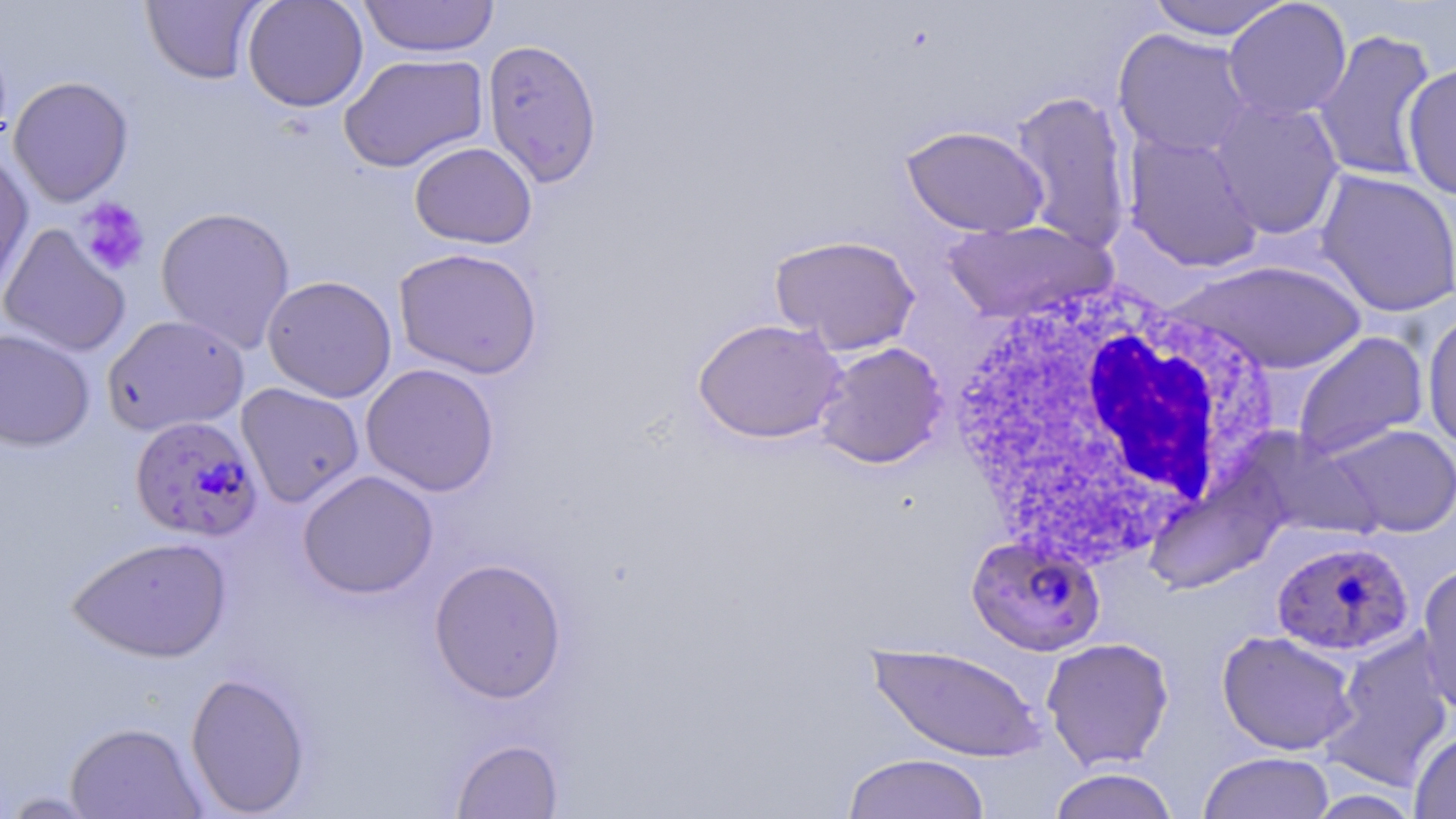 Approximate bounding boxes as (x1, y1, x2, y2) in pixels. White blood cell locations: (941, 271, 1284, 572). Plasmodium falciparum-infected red blood cell locations: (124, 415, 258, 542), (966, 533, 1106, 656), (1271, 539, 1414, 657). Uninfected red blood cell locations: (140, 0, 267, 85), (242, 0, 368, 112), (358, 0, 500, 58), (1147, 0, 1294, 40), (1222, 0, 1352, 121), (1112, 28, 1254, 159), (1311, 28, 1438, 183), (481, 39, 603, 188), (339, 52, 489, 173), (1401, 62, 1456, 201), (8, 76, 134, 207), (1010, 89, 1134, 254), (1208, 98, 1346, 239), (901, 124, 1049, 237), (1123, 131, 1264, 273), (409, 142, 537, 249), (0, 150, 35, 302), (1315, 169, 1456, 317), (155, 206, 296, 354), (941, 220, 1115, 324), (0, 224, 132, 357), (769, 234, 921, 355), (393, 247, 543, 379), (1176, 259, 1367, 374), (262, 275, 397, 402), (1422, 309, 1456, 449), (102, 314, 249, 436), (692, 317, 847, 444), (0, 327, 96, 451), (1292, 330, 1429, 461), (813, 341, 948, 469), (360, 363, 500, 497), (236, 382, 365, 508), (1326, 423, 1456, 537), (297, 470, 439, 599), (68, 535, 232, 663), (428, 557, 567, 703), (1415, 561, 1456, 718), (1216, 629, 1361, 756), (1322, 631, 1455, 790), (1041, 636, 1175, 770), (867, 642, 1047, 762), (185, 671, 311, 816), (64, 721, 207, 818), (1409, 729, 1456, 819), (451, 738, 563, 819), (1198, 751, 1335, 819), (841, 753, 992, 819), (1046, 768, 1180, 819), (2, 791, 104, 817). Platelet locations: (77, 198, 150, 275). Slide-level diagnosis: Plasmodium falciparum. Image is 1456×819 pixels. Captured at 1000x magnification. Optical microscopy. Thin blood film. May-Grünwald-Giemsa stain. One field of a larger specimen.